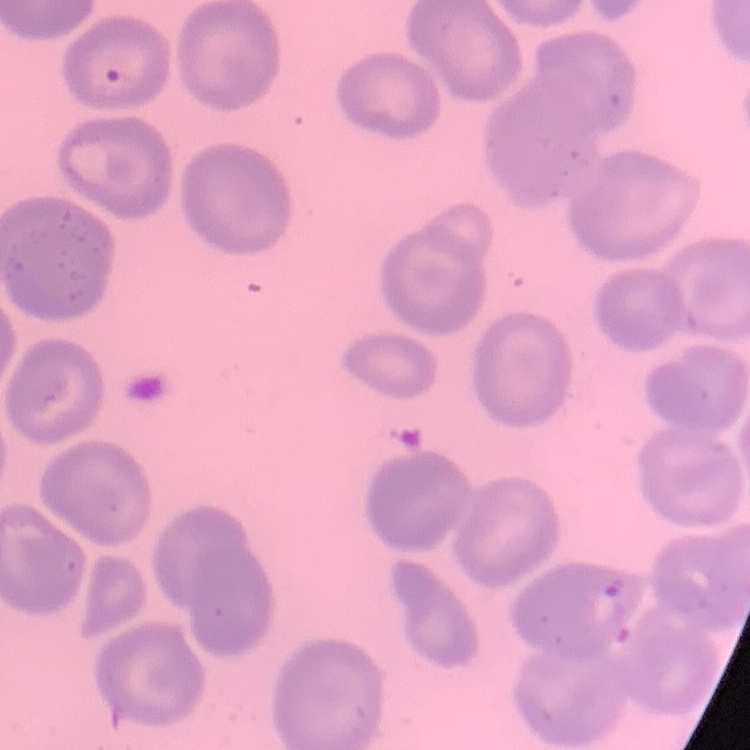

erythrocyte_morphology: no rouleaux formation
image_type: square crop of a larger photomicrograph
preparation: thin peripheral smear
stain: Field's or Giemsa